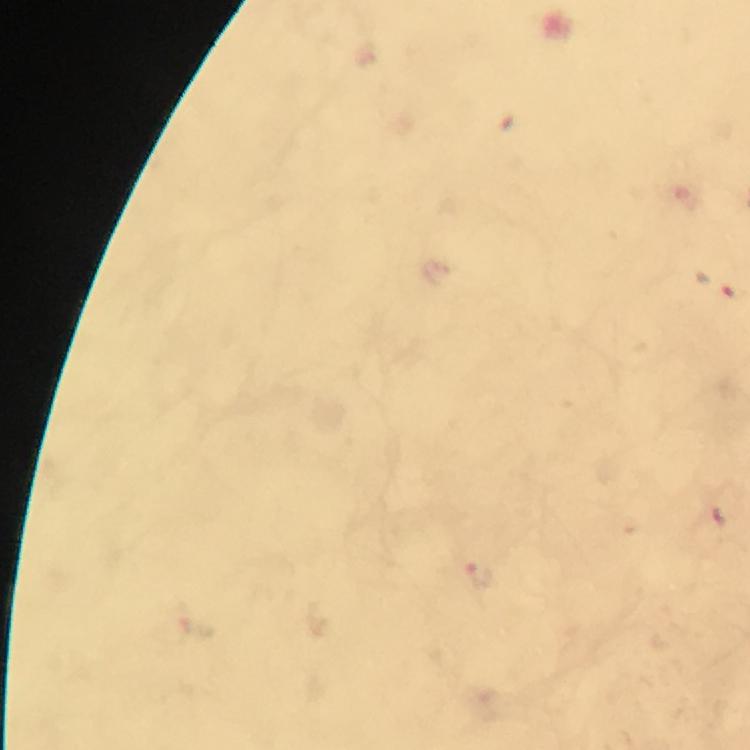 Approximate centers as [x, y] in pixels. Malaria parasite locations: [479, 574]. Immersion oil applied. From a malaria diagnostic workup. Image is 750×750 pixels. Smartphone photograph taken through a microscope. 100x magnification. A crop from one field of view. Giemsa stain. Thick blood film.